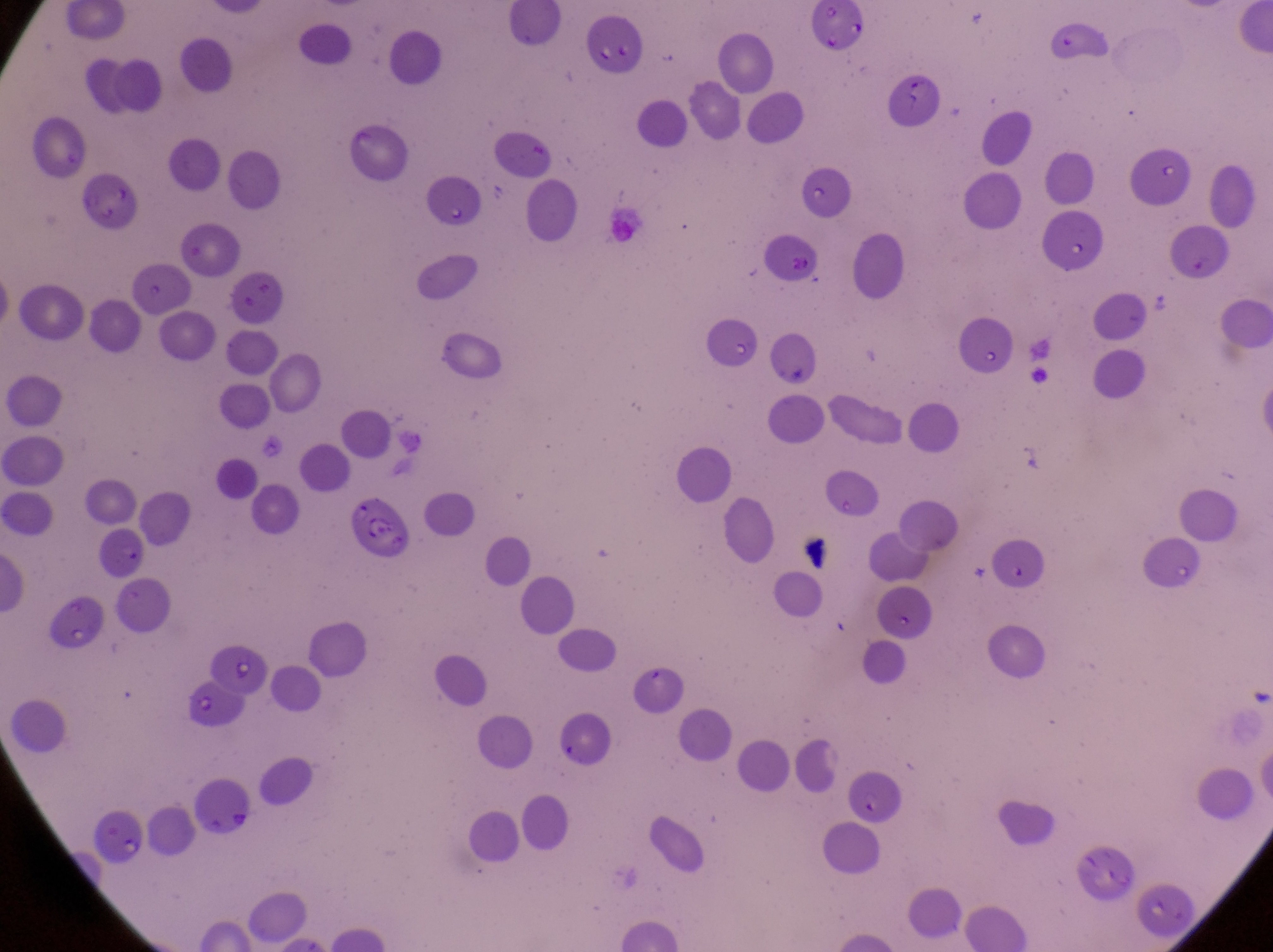
Approximate bounding boxes as [left, top, right, bottom] in pixels.
Summary:
  - Parasitised red blood cell locations: [342, 492, 417, 566], [97, 524, 150, 582], [846, 766, 903, 829]
  - Artifact (platelet-like body, stain precipitate, or debris) locations: [804, 530, 843, 582]
  - Field of view: single
  - Image size: 1273×952 pixels
  - Magnification: 1000x
  - Country: Uganda
  - Preparation: thin blood film
  - Capture: smartphone photograph through the eyepiece of an Olympus CX-23 microscope